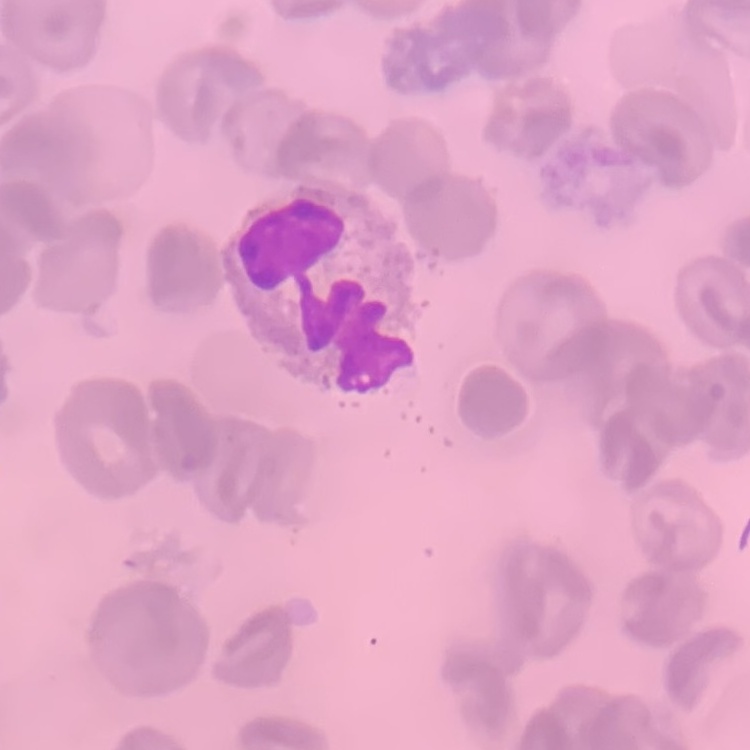
The red blood cells exhibit no rouleaux formation. Stained with either Field's or Giemsa. Thin blood film. One tile cut from a larger photomicrograph.